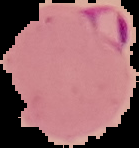
Summary:
  - Image type: segmented cell region with the area outside set to black
  - Image size: 139×148 pixels
  - Preparation: thin blood film
  - Malaria status: parasitized